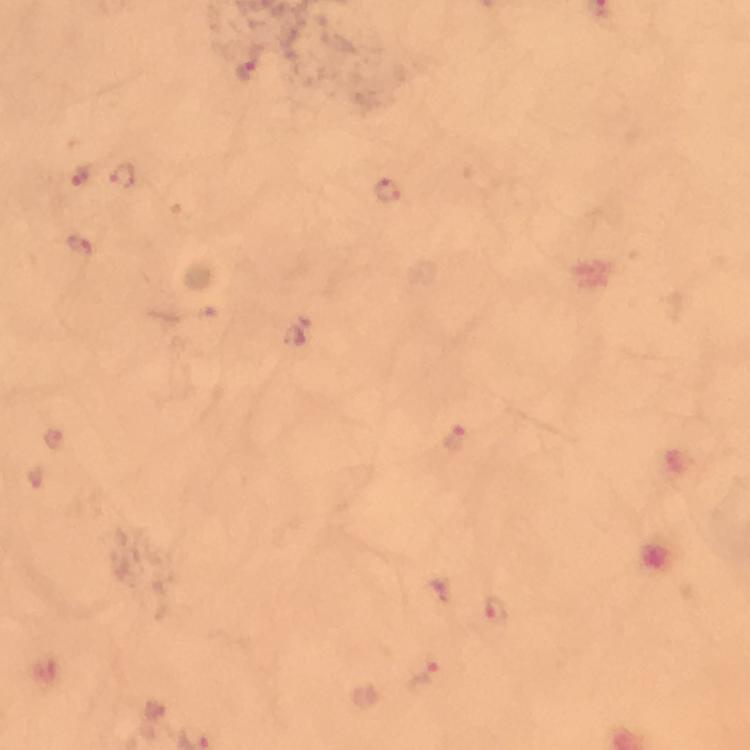

Approximate object centers, in pixels from the top-left corner.
Summary:
  - Malaria parasite locations: (x=247, y=63), (x=81, y=174), (x=125, y=175), (x=387, y=191), (x=78, y=246), (x=455, y=438), (x=496, y=610), (x=427, y=677)
  - Magnification: 100x
  - Image size: 750×750 pixels
  - Immersion oil: used
  - Capture: smartphone photograph through a microscope
  - Context: from a malaria diagnostic workup
  - Cropped from: a single field of view
  - Stain: Giemsa
  - Preparation: thick smear